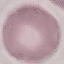
malaria status = uninfected
stain = Giemsa
preparation = thin blood film
capture = smartphone camera at the microscope eyepiece
image type = cell patch, automatically extracted from a larger field of view and resized to 64 × 64 pixels